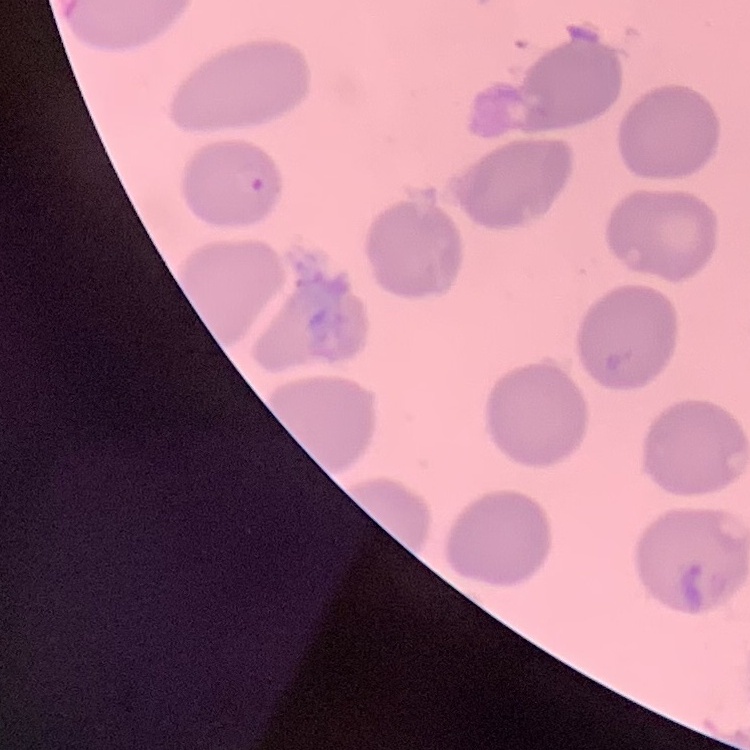

{
  "erythrocyte_morphology": "no rouleaux formation",
  "stain": "Field's or Giemsa",
  "image_type": "square crop of a larger photomicrograph",
  "preparation": "thin peripheral smear"
}